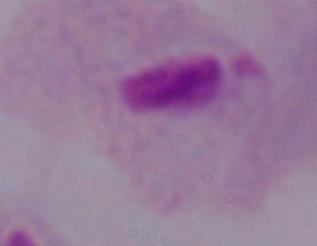
Summary:
  - Modality: photomicrograph
  - Identification: trichomonad
  - Magnification: 1000x